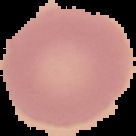
Summary:
  - Preparation: thin blood film
  - Image type: segmented cell region with the area outside set to black
  - Malaria status: uninfected
  - Image size: 136×136 pixels